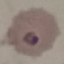
malaria status = parasitized
stain = Giemsa
preparation = thin blood smear
capture = smartphone through the microscope eyepiece
image type = automatically extracted cell patch, resized to 64 × 64 pixels